Assess this cell for malaria.
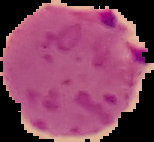
It is parasitized.

Image is 154×142 pixels. Cell region segmented out of the field of view; the surrounding area is masked to black. From a thin blood smear.